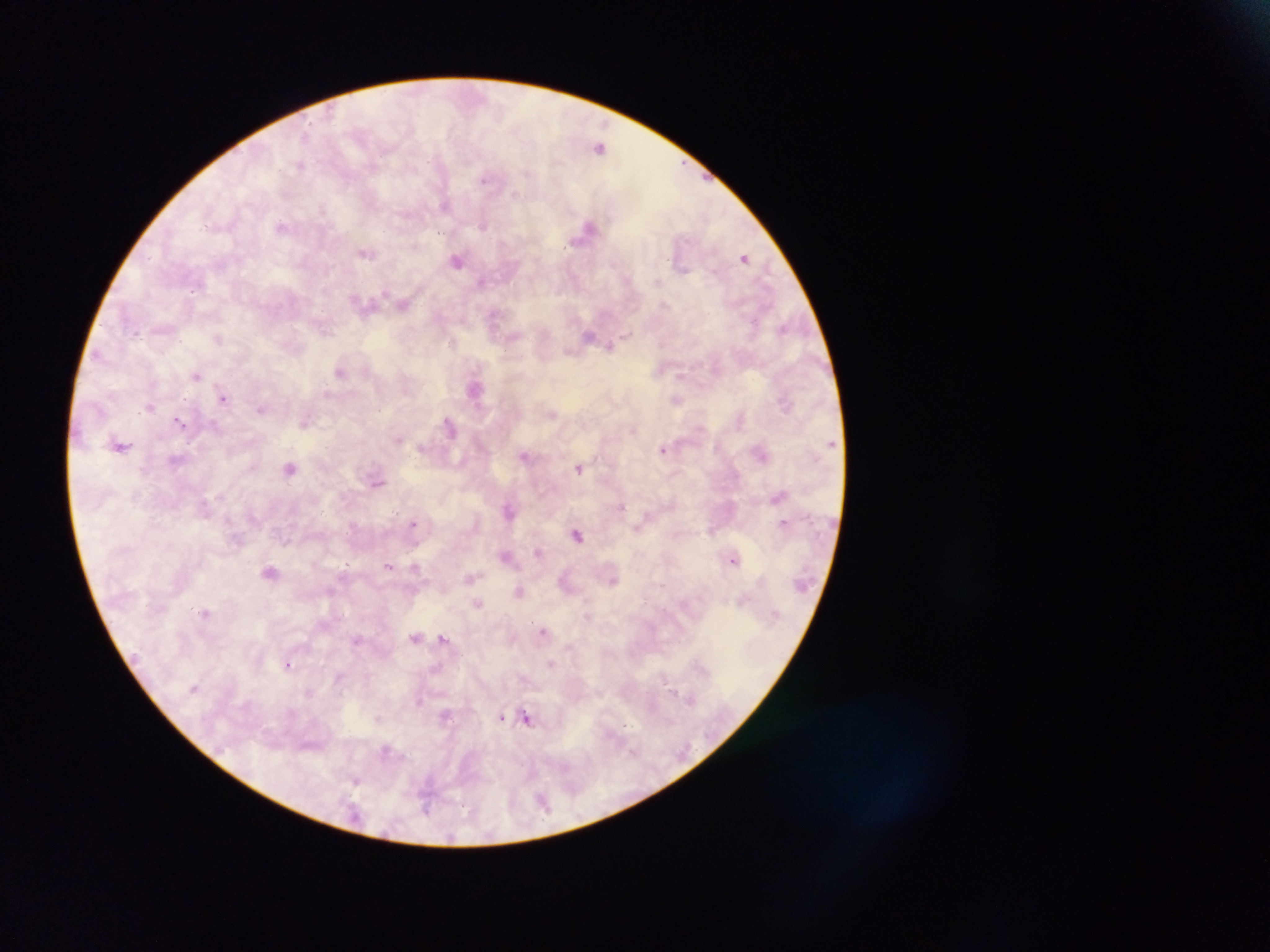
{
  "country": "Ghana",
  "image_size": "1270×952 pixels",
  "malaria_parasite_locations": "approximate centers as x y in pixels: 306 135; 600 145; 301 164; 529 173; 485 179; 515 192; 322 209; 482 224; 589 224; 282 226; 415 243; 363 254; 745 257; 456 261; 657 282; 357 302; 666 304; 591 334; 627 336; 218 338; 452 344; 609 346; 569 351; 340 373; 196 374; 679 375; 475 388; 328 395; 225 399; 678 400; 784 405; 262 410; 178 419; 741 419; 448 420; 304 422; 450 428; 399 438; 422 448; 663 448; 762 453; 526 455; 290 468; 579 468; 378 482; 777 494; 214 495; 621 506; 507 509; 785 521; 414 522; 712 531; 577 533; 538 552; 733 559; 346 566; 389 566; 416 567; 267 572; 472 577; 615 581; 660 585; 330 592; 518 592; 742 600; 477 603; 205 611; 588 613; 544 630; 415 636; 441 637; 569 646; 551 663; 289 665; 700 665; 704 670; 674 692; 677 697; 691 700; 418 702; 503 718; 378 719; 528 720; 354 779",
  "preparation": "thick blood smear",
  "field_of_view": "single",
  "capture": "mobile-phone photograph through a microscope"
}